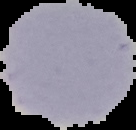
From a thin blood smear. Segmented cell region on a black background. Result: no malaria parasites detected. Image is 136×130 pixels.